Report the malaria status of this cell.
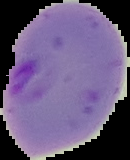
It is parasitized.

From a thin blood film. Image is 130×160 pixels. Cell region segmented out of the field of view; the surrounding area is masked to black.